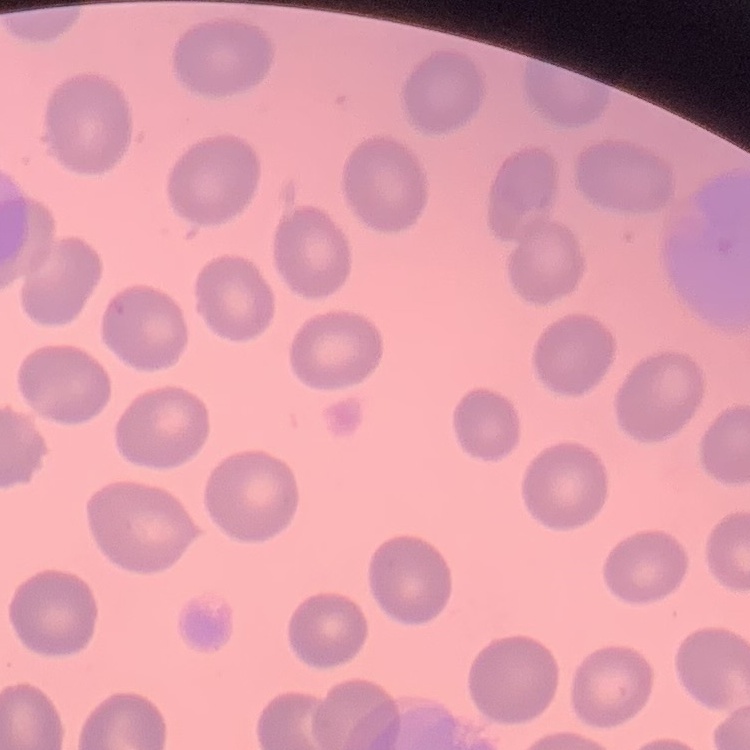
erythrocyte_morphology: no rouleaux formation
stain: Field's or Giemsa
image_type: one tile cut from a larger photomicrograph
preparation: thin blood film